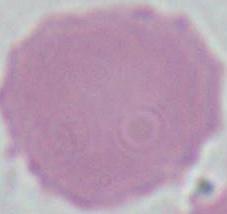
magnification = 1000x
modality = micrograph
identification = erythrocyte